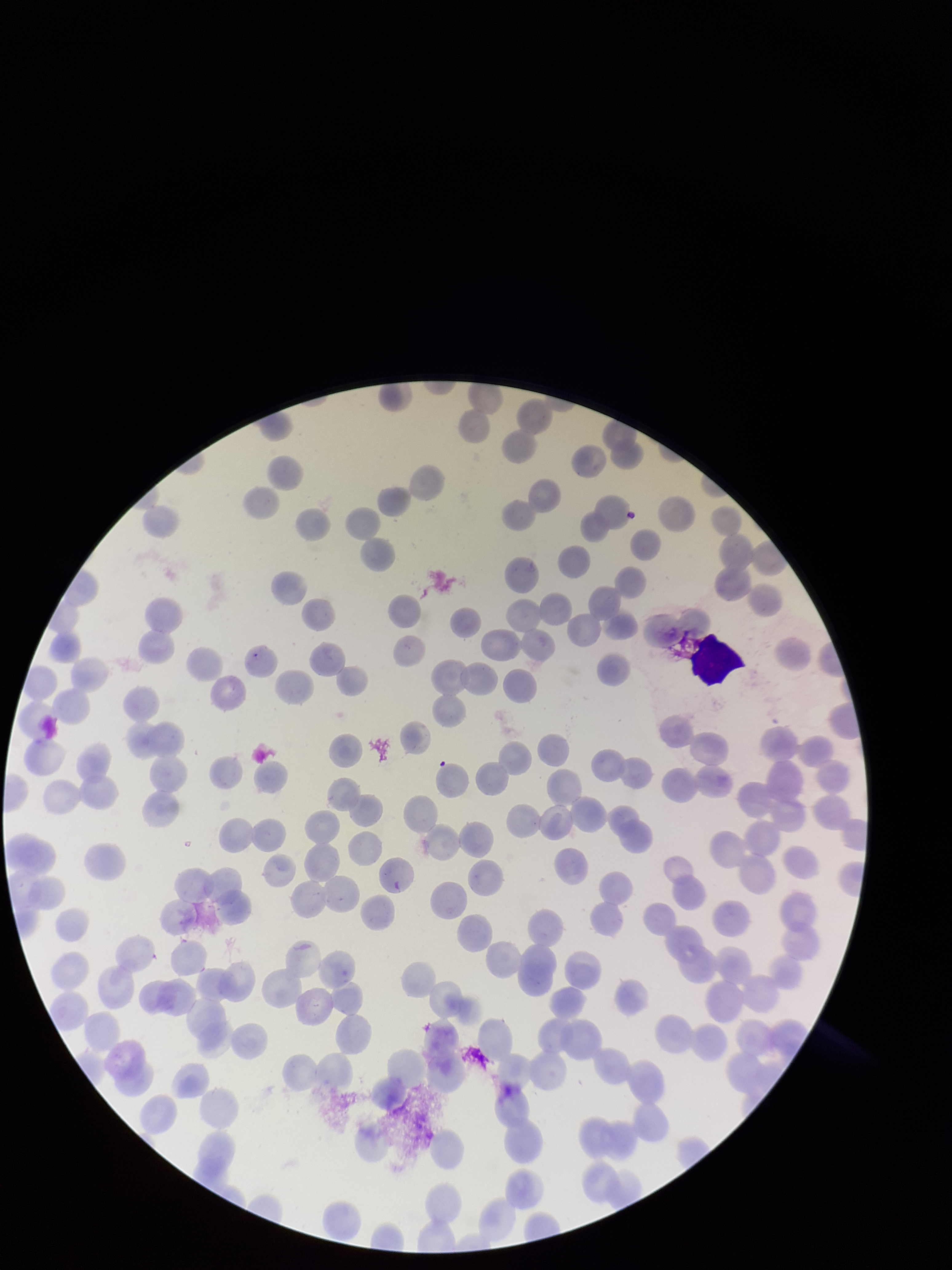

Summary:
  - Stain: Giemsa
  - Capture: smartphone photograph through the microscope eyepiece
  - Species reported for this patient: Plasmodium falciparum
  - Preparation: thin smear
  - Parasitized red blood cell count: 0
  - Patient malaria status: infected
  - Parasitized red blood cells: none seen
  - Image size: 952×1270 pixels
  - Field of view: single
  - Red blood cell count: 200